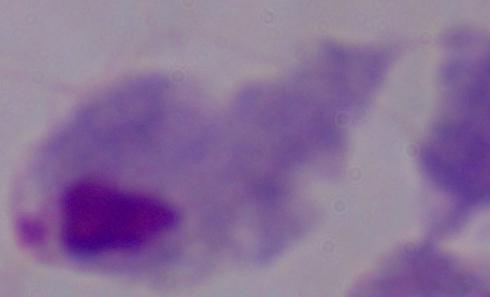

1000x magnification. A trichomonad is seen. Photomicrograph.